Assess this cell for malaria.
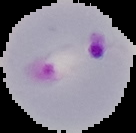
Parasitized.

preparation = thin blood smear
image size = 136×133 pixels
image type = segmented cell region with the area outside set to black